Assess the morphology of the erythrocytes.
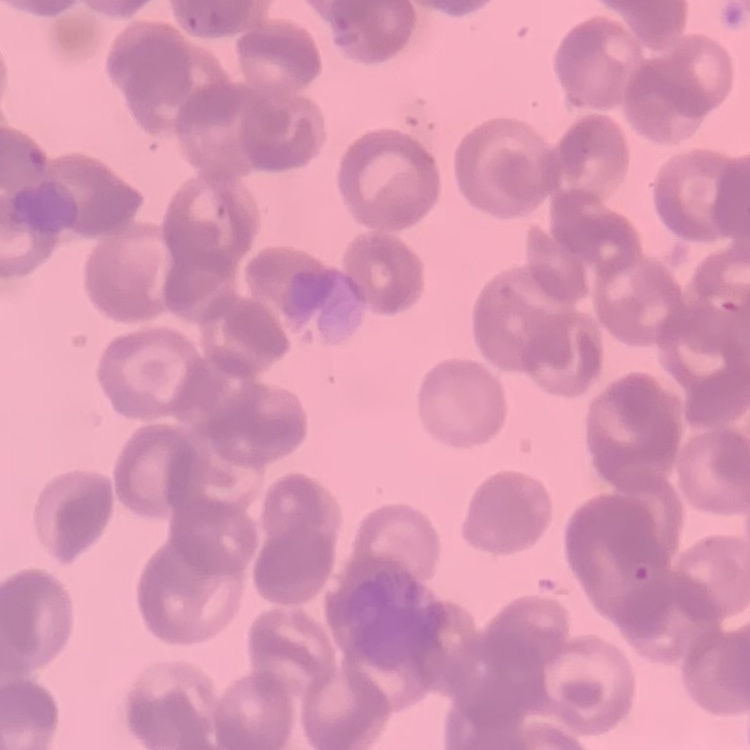

Rouleaux formation.

Summary:
  - Image type: one tile cut from a larger photomicrograph
  - Preparation: thin peripheral smear
  - Stain: Field's or Giemsa